Classify this cell by malaria status.
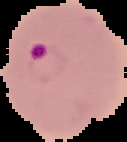
Parasitized.

Image is 127×142 pixels. From a thin blood film. Segmented cell region on a black background.